Report the malaria status.
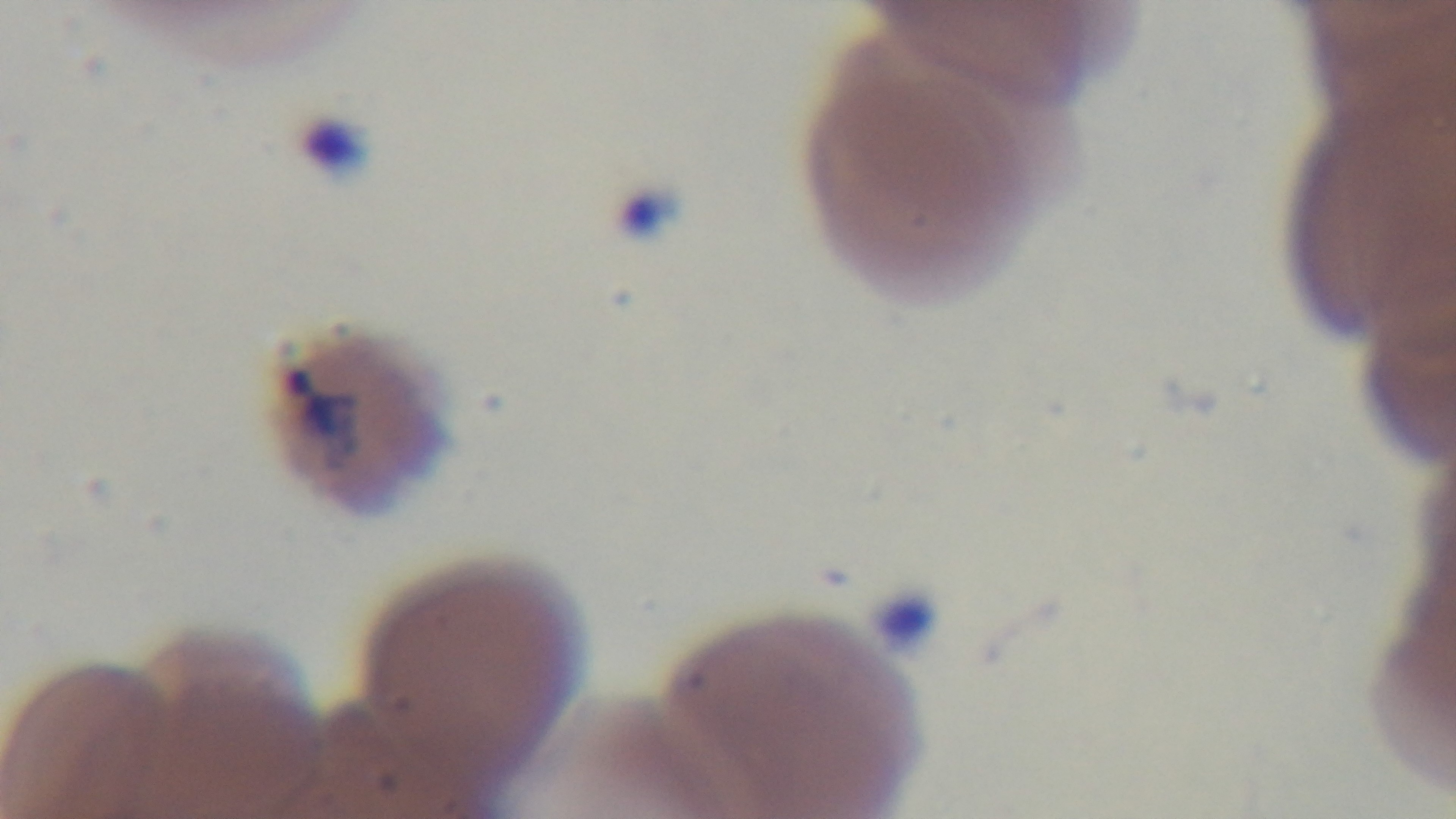

Infected.

{
  "field_of_view": "one from the slide",
  "stain": "Giemsa",
  "preparation": "thin smear",
  "modality": "light microscopy",
  "objective": "100x oil immersion",
  "capture": "mounted 4K digital camera"
}